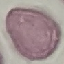

result = negative for malaria parasites
capture = smartphone through the microscope eyepiece
preparation = thin blood film
image type = cell patch, automatically extracted from a larger field of view and resized to 64 × 64 pixels
stain = Giemsa